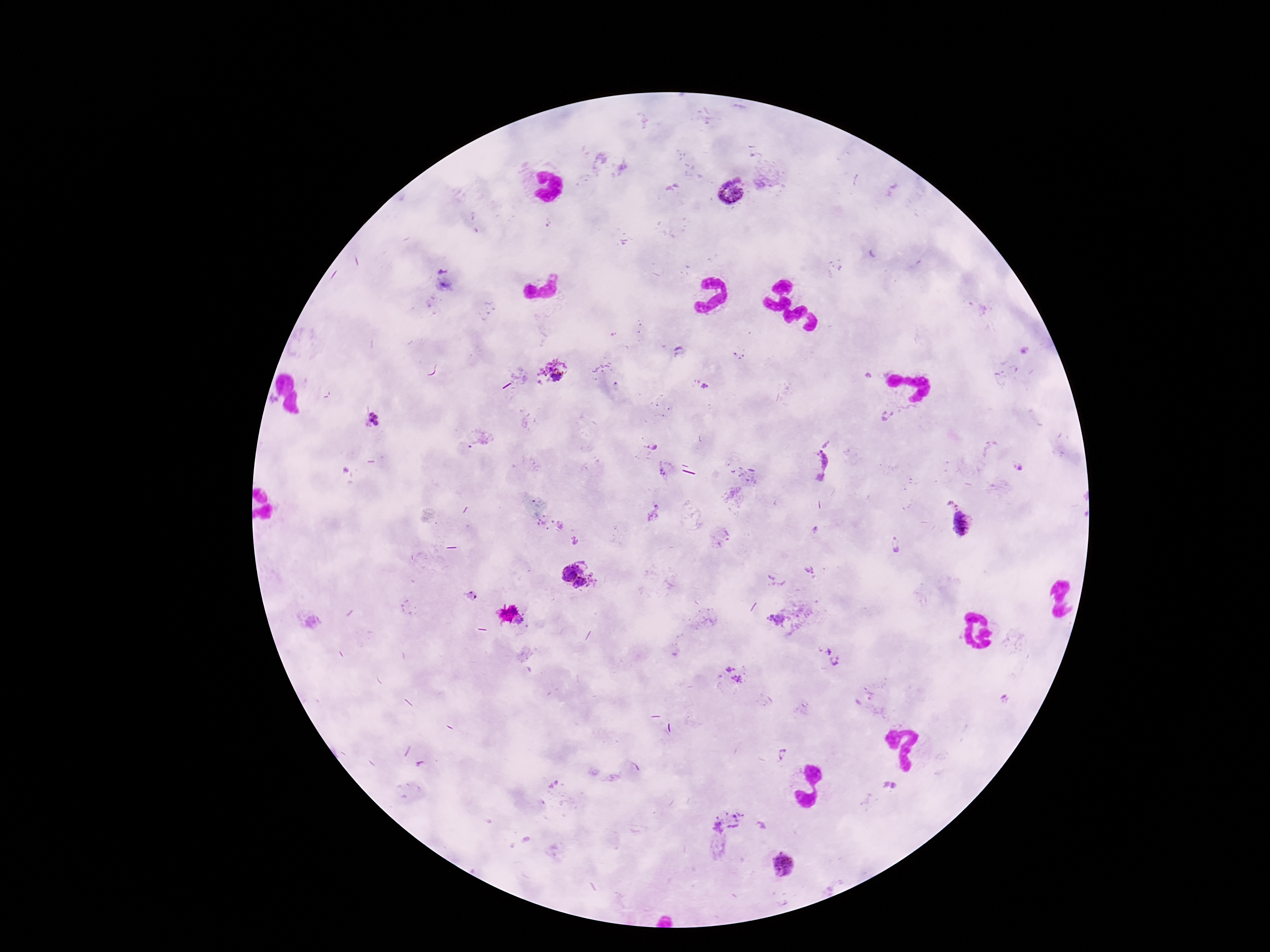
Approximate centers as [x, y] in pixels. Plasmodium parasite locations: [730, 191], [680, 351], [553, 371], [867, 376], [703, 384], [886, 415], [372, 421], [827, 444], [652, 447], [818, 465], [1018, 467], [664, 469], [952, 506], [655, 514], [545, 522], [561, 524], [962, 524], [815, 529], [575, 541], [895, 544], [581, 567], [809, 570], [569, 573], [593, 577], [581, 585], [471, 597], [776, 618], [825, 652], [836, 660], [727, 669], [735, 670], [738, 679], [1004, 699], [781, 754], [885, 784], [895, 785], [728, 821], [761, 826], [782, 864]. Smartphone photograph taken through the microscope eyepiece. 100x magnification. Giemsa stain. One field from this slide. Image is 1270×952 pixels. Patient malaria status: positive. Thick blood film.